Locate every malaria parasite.
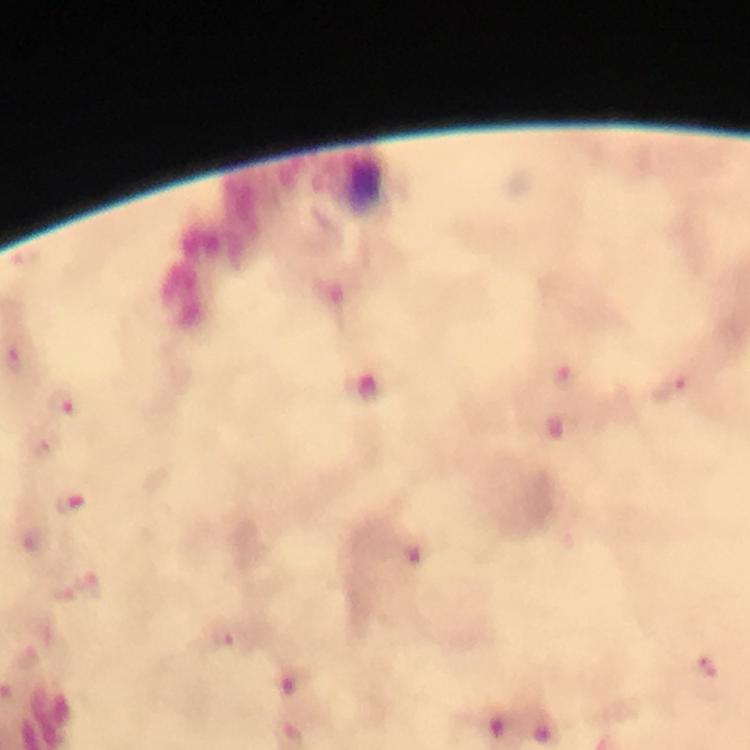

Approximate centers as {x, y} in pixels.
Malaria parasites: {670, 392}, {67, 403}, {47, 448}, {71, 505}, {228, 637}, {712, 666}.

stain = Giemsa
context = from a diagnostic examination for malaria
image size = 750×750 pixels
immersion oil = used
magnification = 100x
cropped from = one field of view
capture = smartphone mounted on the microscope
preparation = thick smear